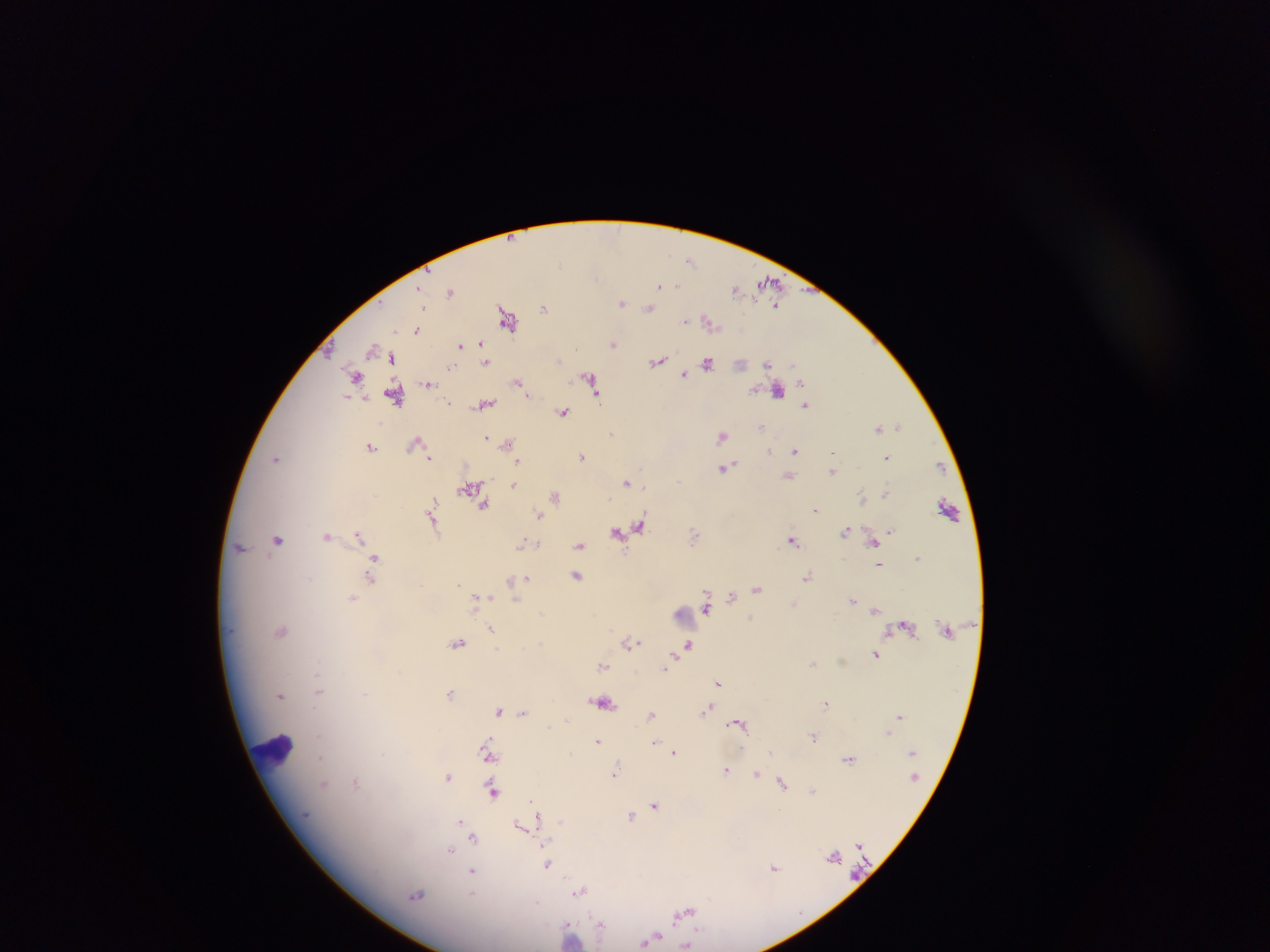
Approximate centers as {x, y} in pixels. Plasmodium parasite locations: {691, 260}, {559, 264}, {769, 281}, {660, 285}, {735, 288}, {451, 292}, {621, 303}, {777, 305}, {422, 307}, {544, 308}, {648, 308}, {507, 319}, {684, 320}, {708, 321}, {417, 329}, {613, 344}, {481, 345}, {460, 346}, {373, 348}, {392, 357}, {486, 361}, {658, 361}, {708, 363}, {768, 364}, {452, 366}, {683, 375}, {356, 376}, {590, 380}, {518, 382}, {429, 383}, {801, 383}, {777, 391}, {396, 394}, {528, 394}, {450, 403}, {484, 404}, {805, 404}, {562, 411}, {898, 426}, {761, 427}, {878, 429}, {611, 434}, {722, 435}, {486, 438}, {508, 442}, {415, 443}, {370, 447}, {769, 451}, {795, 451}, {833, 453}, {581, 456}, {430, 457}, {887, 457}, {276, 459}, {518, 461}, {725, 467}, {939, 467}, {833, 472}, {788, 476}, {626, 482}, {514, 485}, {470, 488}, {887, 493}, {555, 496}, {863, 498}, {484, 505}, {432, 508}, {948, 508}, {816, 510}, {539, 516}, {433, 523}, {641, 527}, {890, 530}, {846, 531}, {618, 532}, {695, 535}, {326, 536}, {358, 536}, {277, 539}, {792, 540}, {873, 542}, {522, 544}, {539, 544}, {580, 546}, {239, 548}, {918, 558}, {374, 559}, {880, 564}, {577, 576}, {808, 576}, {371, 578}, {526, 579}, {512, 582}, {460, 585}, {757, 588}, {514, 589}, {482, 598}, {732, 598}, {352, 599}, {516, 600}, {853, 600}, {706, 607}, {875, 609}, {491, 628}, {281, 631}, {630, 642}, {458, 644}, {688, 645}, {876, 654}, {812, 663}, {602, 665}, {665, 668}, {317, 675}, {719, 683}, {318, 692}, {451, 693}, {365, 694}, {280, 695}, {603, 702}, {826, 703}, {706, 710}, {499, 711}, {523, 712}, {652, 715}, {899, 715}, {567, 718}, {737, 723}, {888, 733}, {814, 736}, {318, 737}, {597, 741}, {654, 741}, {488, 745}, {771, 752}, {674, 753}, {570, 754}, {490, 755}, {319, 759}, {849, 759}, {726, 769}, {616, 771}, {756, 774}, {448, 777}, {782, 783}, {323, 784}, {356, 784}, {493, 791}, {813, 791}, {533, 804}, {655, 806}, {631, 815}, {538, 817}, {460, 822}, {521, 825}, {474, 838}, {450, 850}, {834, 856}, {546, 864}, {774, 868}, {473, 871}, {580, 891}, {418, 895}, {684, 913}, {601, 924}, {571, 936}, {651, 938}, {687, 945}. Leukocyte locations: {686, 616}, {273, 753}. Collected in Ghana. Image is 1270×952 pixels. Single field of view. Thick blood film. Mobile-phone photograph taken through the microscope.